Identify the parasite.
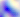

Toxoplasma gondii.

modality: photomicrograph
magnification: 400x